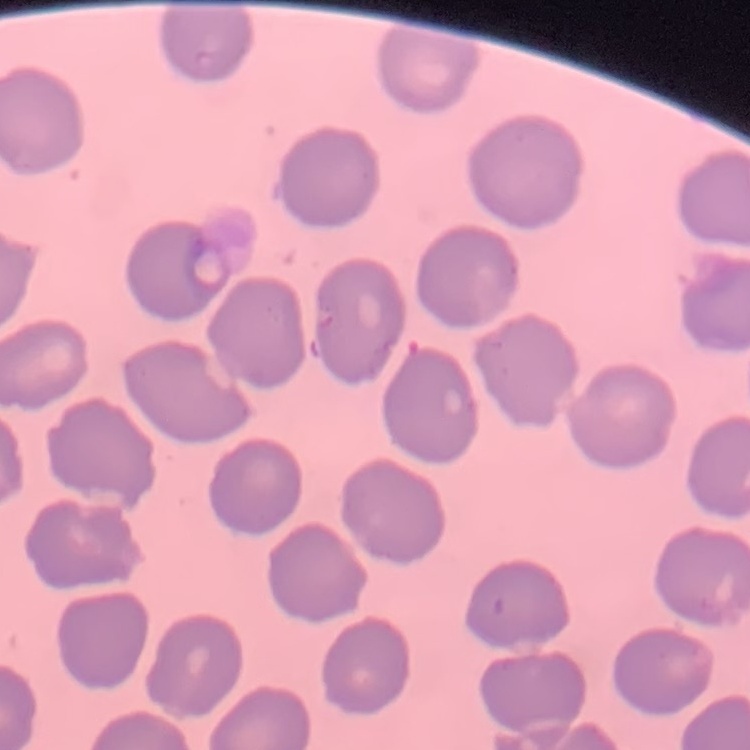

The red blood cells exhibit no rouleaux formation. One tile cut from a larger photomicrograph. Field's or Giemsa stain. Thin blood film.